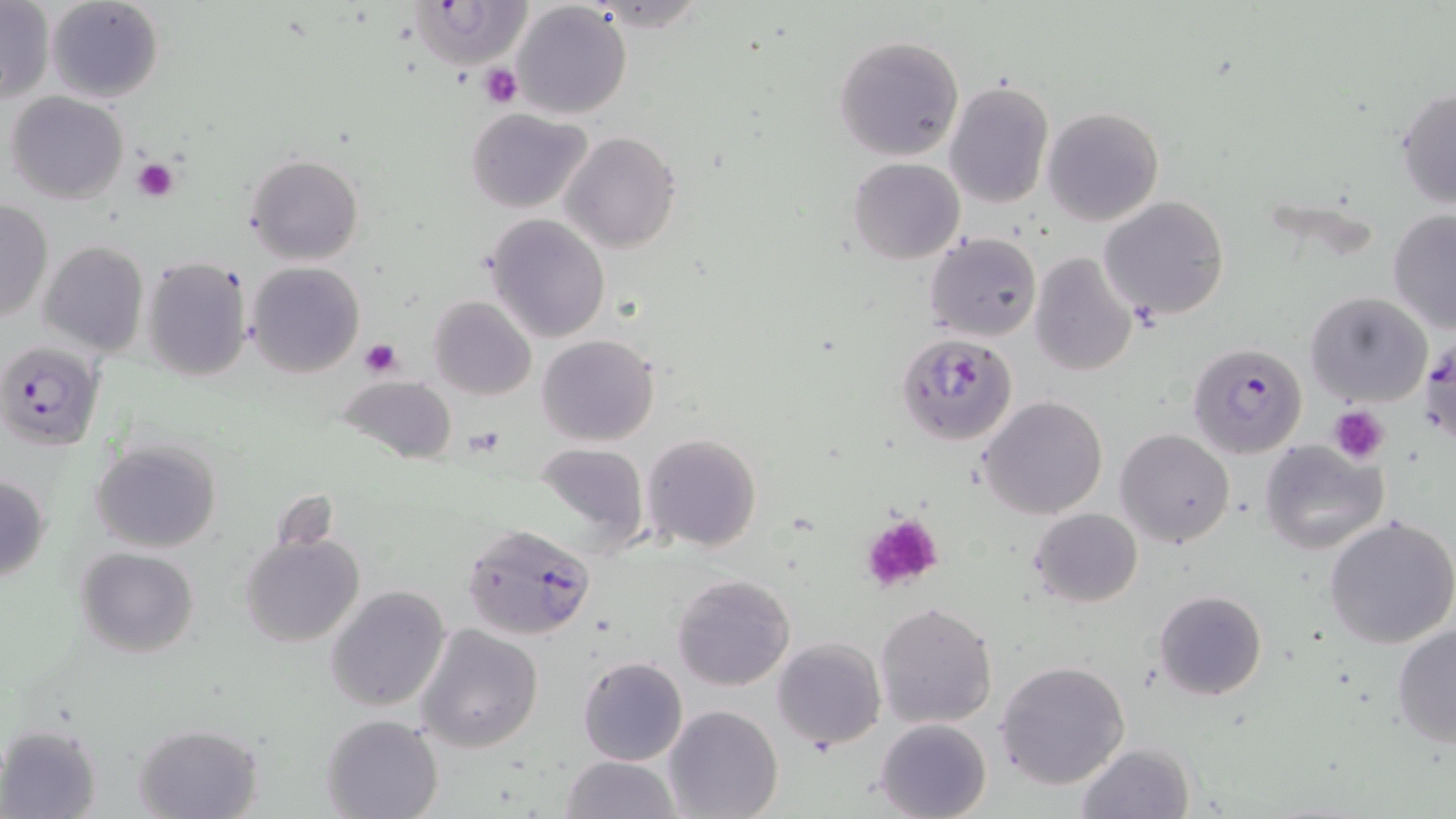 Approximate bounding boxes as (x1,y1)-(x2,y2) corner pairs in pixels. Plasmodium falciparum-infected red blood cell locations: (892,331)-(1016,445), (1420,334)-(1456,444), (1,340)-(105,451), (1186,342)-(1307,458), (463,524)-(596,641). Platelet locations: (480,64)-(523,108), (134,158)-(179,201), (360,339)-(403,377), (1329,406)-(1389,463), (859,513)-(944,593). Uninfected red blood cell locations: (45,0)-(163,103), (405,2)-(532,71), (511,2)-(632,118), (0,3)-(53,104), (833,35)-(964,161), (943,81)-(1053,209), (1395,87)-(1455,210), (6,93)-(128,205), (1041,106)-(1164,226), (466,107)-(590,213), (560,130)-(681,253), (244,153)-(364,265), (848,157)-(965,264), (1099,194)-(1229,321), (0,199)-(52,324), (1387,210)-(1456,337), (486,214)-(611,343), (925,232)-(1042,342), (38,240)-(148,359), (1029,252)-(1137,376), (142,256)-(253,383), (245,261)-(365,379), (1305,291)-(1433,408), (428,295)-(536,400), (537,334)-(659,447), (338,375)-(456,464), (977,395)-(1109,520), (1115,427)-(1235,548), (641,432)-(763,553), (1259,438)-(1389,556), (90,440)-(222,552), (534,440)-(650,553), (0,473)-(51,583), (1031,508)-(1142,607), (1324,514)-(1456,650), (239,531)-(365,649), (74,546)-(199,657), (673,573)-(797,692), (327,585)-(452,713), (1153,589)-(1267,700), (874,602)-(999,729), (416,624)-(543,752), (1391,624)-(1456,747), (773,637)-(886,750), (577,656)-(688,765), (994,660)-(1132,789), (663,705)-(782,819), (322,714)-(444,819), (875,717)-(992,819), (133,723)-(262,818), (1,725)-(102,818), (1075,742)-(1196,819), (561,755)-(681,819). Slide-level diagnosis: Plasmodium falciparum. 1000x magnification. One field of a larger specimen. Thin blood film. Optical microscopy. Image is 1456×819 pixels. May-Grünwald-Giemsa stain.